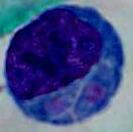 A leukocyte is seen. Captured at 1000x magnification. Micrograph.